Give the preparation type.
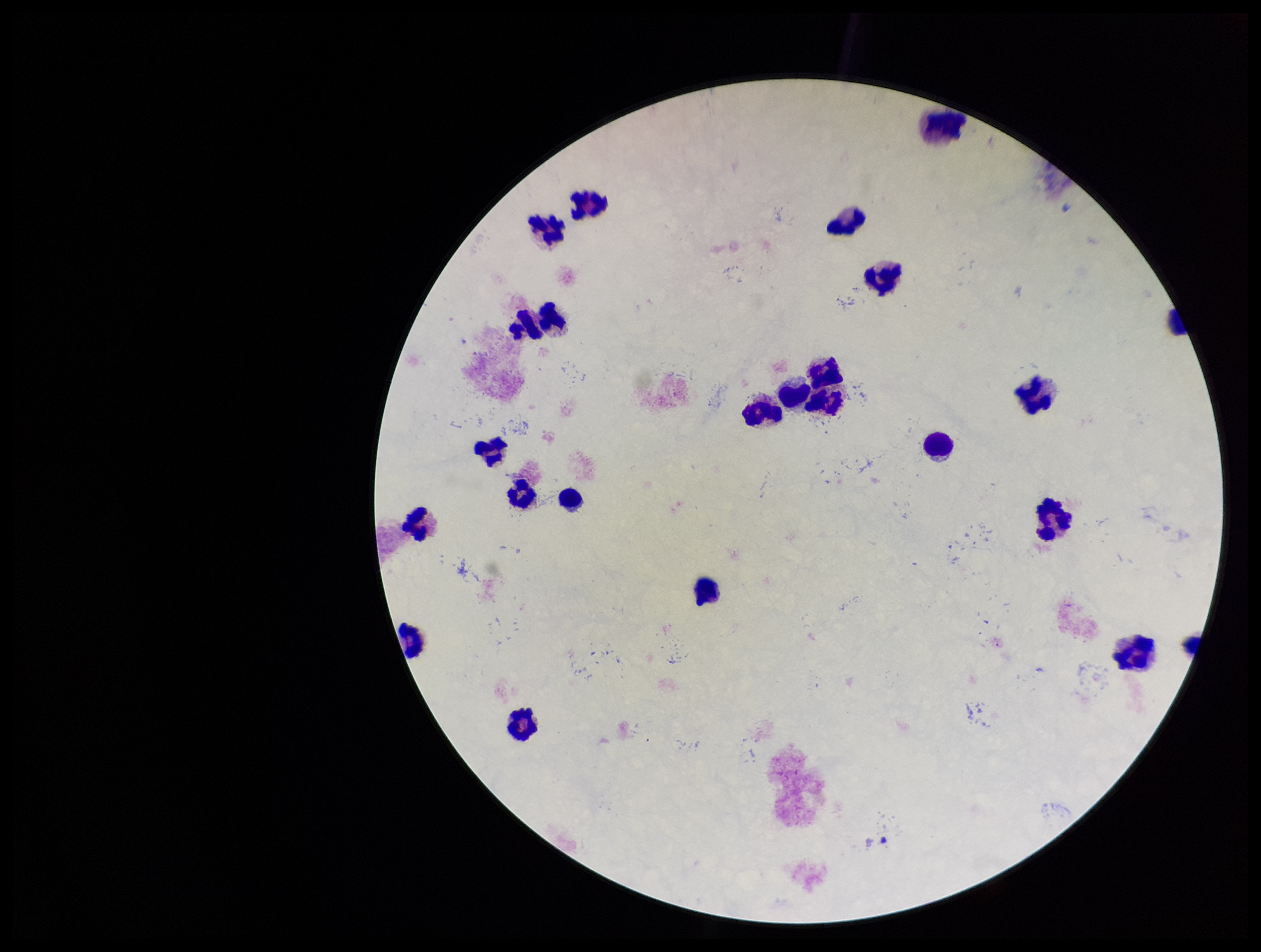
Thick.

Summary:
  - Leukocyte count: 22
  - Capture: smartphone photograph through the microscope eyepiece
  - Image size: 1261×952 pixels
  - Plasmodium parasites: none detected
  - Field of view: single
  - Patient malaria status: negative
  - Stain: Giemsa
  - Parasite count: 0